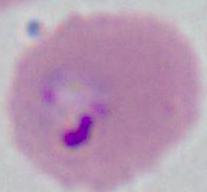

magnification = 400x or 1000x
identification = Plasmodium
modality = photomicrograph